Which red blood cells are P. falciparum-infected, and which are of indeterminate infection status?
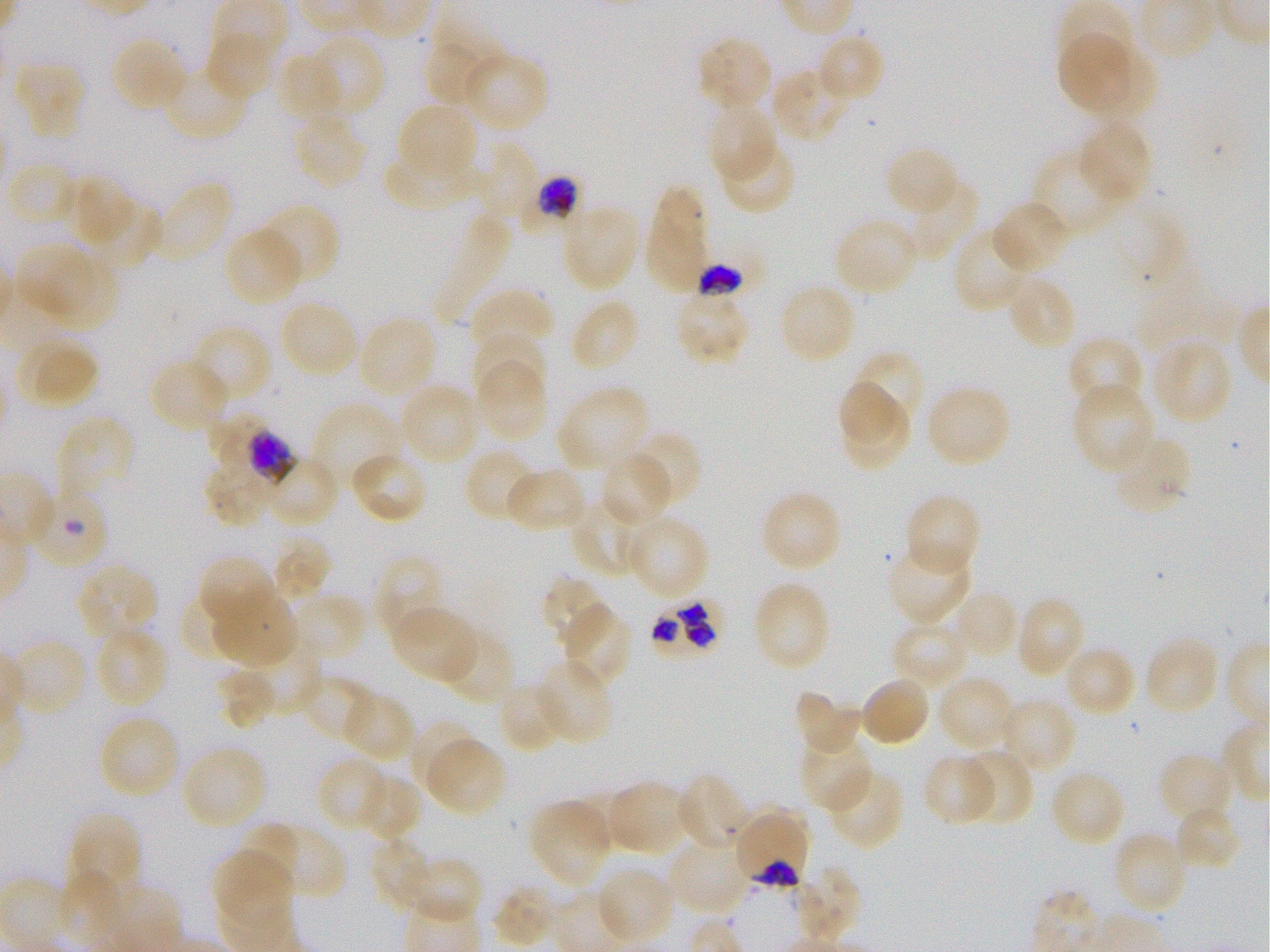
Approximate bounding boxes as (x1, y1, x2, y2) in pixels. Not every red blood cell is marked. A life-cycle stage — or a range of stages, where the recorded stages span more than one — follows each staged infected red blood cell.
Infected red blood cells: (522, 174, 584, 231) schizont; (696, 241, 771, 298); (216, 421, 294, 488) late trophozoite to early schizont; (649, 593, 729, 664); (733, 807, 810, 889) trophozoite.
Red blood cells of indeterminate infection status: (26, 483, 110, 571).

locations of uninfected red blood cells = (204, 28, 279, 101), (424, 28, 506, 109), (815, 31, 884, 104), (298, 33, 384, 120), (1058, 33, 1132, 111), (696, 35, 776, 112), (110, 36, 190, 113), (277, 51, 350, 129), (461, 51, 549, 134), (11, 62, 86, 140), (161, 63, 249, 142), (770, 66, 854, 144), (707, 100, 778, 183), (396, 102, 479, 184), (293, 109, 369, 188), (1076, 120, 1153, 206), (717, 138, 797, 215), (472, 140, 539, 224), (883, 145, 961, 218), (383, 147, 488, 218), (1032, 148, 1123, 234), (6, 162, 78, 227), (69, 176, 134, 244), (149, 179, 232, 267), (899, 180, 979, 263), (645, 184, 710, 296), (991, 200, 1073, 276), (256, 203, 341, 287), (96, 204, 159, 267), (561, 204, 642, 292), (833, 215, 920, 298), (223, 226, 306, 308), (953, 227, 1035, 314), (15, 243, 95, 315), (42, 259, 118, 331), (1005, 274, 1077, 353), (777, 283, 858, 367), (469, 287, 554, 357), (674, 292, 751, 366), (569, 297, 641, 374), (278, 298, 360, 381), (356, 315, 438, 401), (190, 323, 273, 405), (472, 332, 545, 404), (17, 335, 99, 411), (1066, 336, 1146, 413), (1149, 337, 1233, 427), (846, 350, 926, 433), (149, 358, 230, 434), (474, 358, 548, 444), (836, 378, 907, 445), (398, 381, 481, 468), (1070, 381, 1155, 476), (924, 382, 1013, 469), (556, 383, 651, 475), (310, 402, 400, 492), (839, 403, 914, 473), (54, 415, 135, 505), (625, 430, 702, 511), (1109, 432, 1192, 516), (463, 448, 538, 524), (348, 450, 429, 525), (252, 452, 340, 528), (599, 452, 674, 526), (505, 465, 588, 533), (205, 466, 268, 526), (759, 489, 842, 574), (572, 492, 654, 576), (903, 493, 982, 579), (624, 515, 709, 602), (270, 536, 330, 603), (885, 541, 973, 624), (197, 555, 277, 633), (374, 556, 445, 641), (75, 561, 159, 642), (541, 574, 614, 648), (752, 580, 831, 673), (182, 581, 256, 655), (958, 590, 1020, 655), (287, 593, 368, 663), (214, 594, 297, 668), (1013, 594, 1086, 679), (559, 602, 633, 688), (388, 604, 483, 685), (891, 619, 973, 690), (93, 625, 170, 710), (439, 626, 513, 705), (1144, 635, 1221, 717), (9, 638, 88, 717), (245, 639, 323, 712), (1062, 643, 1139, 718), (534, 660, 611, 747), (217, 668, 277, 730), (297, 674, 371, 738), (859, 675, 932, 748), (935, 675, 1017, 754), (496, 680, 571, 753), (793, 688, 864, 758), (340, 689, 416, 764), (996, 697, 1077, 776), (98, 714, 181, 800), (408, 718, 482, 796), (798, 730, 873, 811), (423, 735, 508, 817), (180, 745, 268, 832), (956, 749, 1034, 828), (1158, 752, 1235, 827), (922, 753, 1000, 827), (317, 755, 391, 833), (824, 767, 904, 850), (1048, 769, 1127, 848), (677, 772, 753, 851), (353, 773, 425, 844), (604, 780, 695, 856), (526, 800, 613, 889), (1174, 804, 1242, 871), (66, 812, 141, 889), (244, 820, 301, 884), (270, 827, 346, 890), (1110, 830, 1190, 914), (367, 837, 438, 914), (665, 837, 755, 916), (213, 849, 293, 930), (391, 854, 482, 925), (593, 865, 676, 946), (793, 866, 862, 945), (491, 885, 564, 948)
life-cycle stages observed = trophozoite, schizont
objective = 100x, oil immersion, numerical aperture 1.25
field of view = single
image size = 1270×952 pixels
preparation = thin blood smear
culture = static in-vitro P. falciparum strain 3D7
stain = Giemsa
donor blood group = O+